Locate and identify every blood parasite.
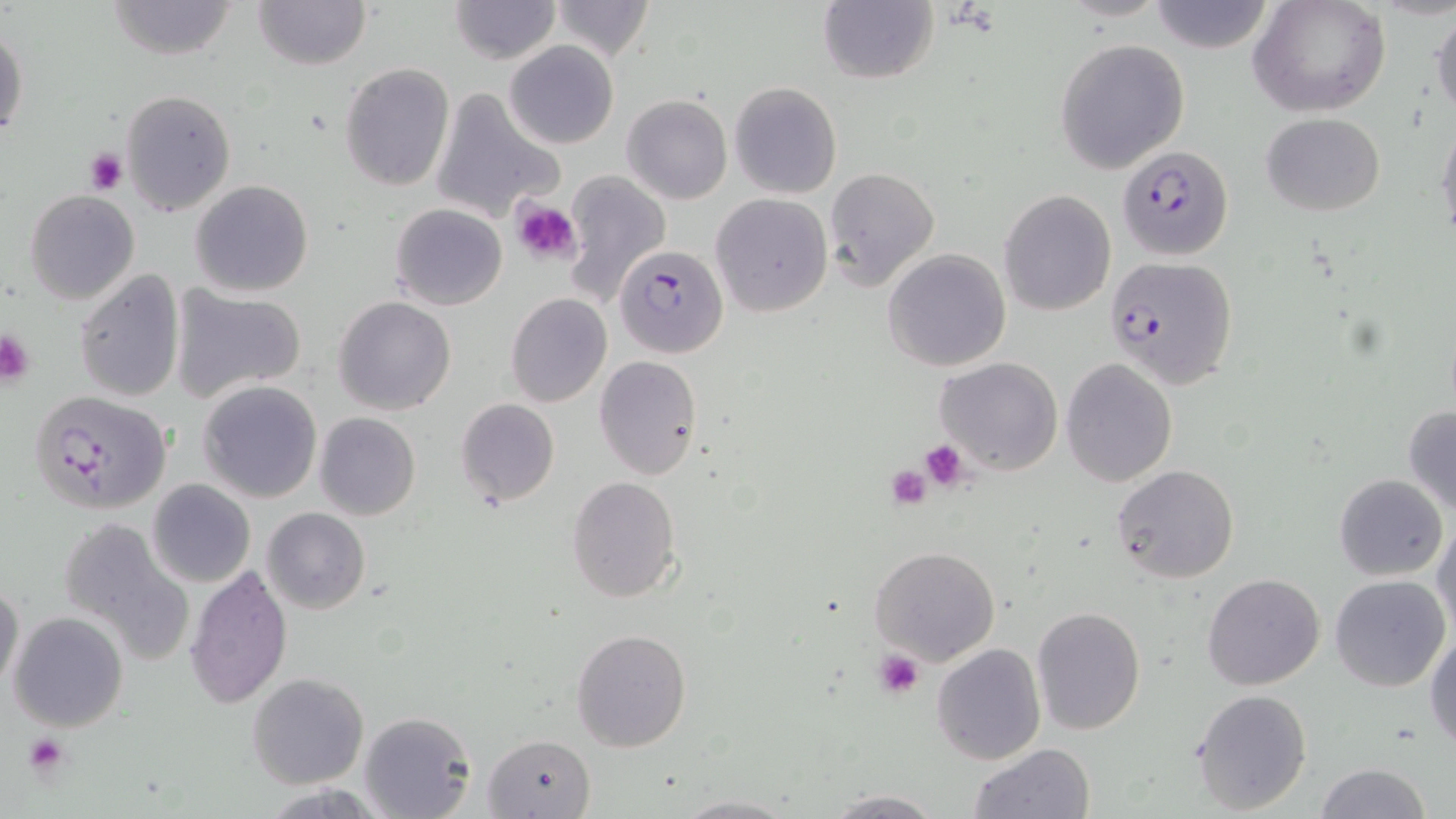
Approximate bounding boxes as (x1, y1, x2, y2) in pixels.
Plasmodium falciparum-infected red blood cells: (1117, 146, 1232, 261), (610, 245, 727, 361), (1105, 255, 1238, 388), (28, 389, 172, 515).
No Plasmodium ovale, Plasmodium malariae, Plasmodium vivax, Babesia divergens, or Trypanosoma brucei observed.

Summary:
  - Platelet locations: (84, 147, 128, 195), (511, 199, 581, 267), (0, 328, 36, 385), (919, 441, 970, 491), (884, 464, 933, 509), (873, 651, 924, 700), (24, 733, 69, 776)
  - Uninfected red blood cell locations: (252, 0, 371, 70), (448, 0, 560, 64), (552, 0, 654, 60), (1149, 0, 1275, 54), (1249, 0, 1390, 117), (105, 1, 241, 60), (816, 1, 937, 86), (1430, 5, 1456, 118), (0, 22, 28, 146), (1054, 38, 1190, 175), (503, 40, 619, 150), (339, 62, 454, 192), (730, 81, 843, 199), (119, 87, 237, 216), (431, 87, 562, 222), (622, 94, 733, 205), (1260, 112, 1387, 216), (1437, 116, 1456, 242), (824, 167, 941, 293), (559, 170, 669, 308), (191, 179, 312, 297), (998, 189, 1116, 317), (24, 190, 140, 306), (712, 193, 833, 316), (390, 202, 507, 310), (883, 249, 1010, 372), (74, 271, 185, 402), (172, 286, 308, 403), (505, 293, 612, 408), (334, 296, 456, 416), (935, 356, 1061, 475), (593, 357, 702, 479), (1061, 359, 1178, 486), (199, 380, 323, 503), (454, 398, 560, 506), (1403, 404, 1456, 517), (315, 413, 420, 521), (1111, 464, 1239, 584), (1333, 473, 1448, 581), (567, 476, 679, 603), (146, 479, 256, 588), (263, 507, 371, 615), (56, 515, 190, 658), (1432, 518, 1456, 640), (868, 545, 1001, 667), (186, 566, 293, 708), (1204, 573, 1325, 690), (1330, 574, 1451, 692), (0, 581, 24, 697), (1031, 605, 1145, 735), (8, 612, 128, 732), (570, 629, 691, 752), (1426, 631, 1456, 751), (932, 644, 1045, 765), (248, 673, 368, 789), (1191, 689, 1314, 815), (360, 712, 476, 819), (484, 734, 597, 817), (966, 743, 1096, 819), (1315, 763, 1432, 819), (822, 790, 946, 817), (670, 792, 799, 817)
  - Slide-level diagnosis: Plasmodium falciparum
  - Image size: 1456×819 pixels
  - Modality: light microscopy
  - Magnification: 1000x
  - Stain: May-Grünwald-Giemsa
  - Preparation: thin blood film
  - Field of view: single